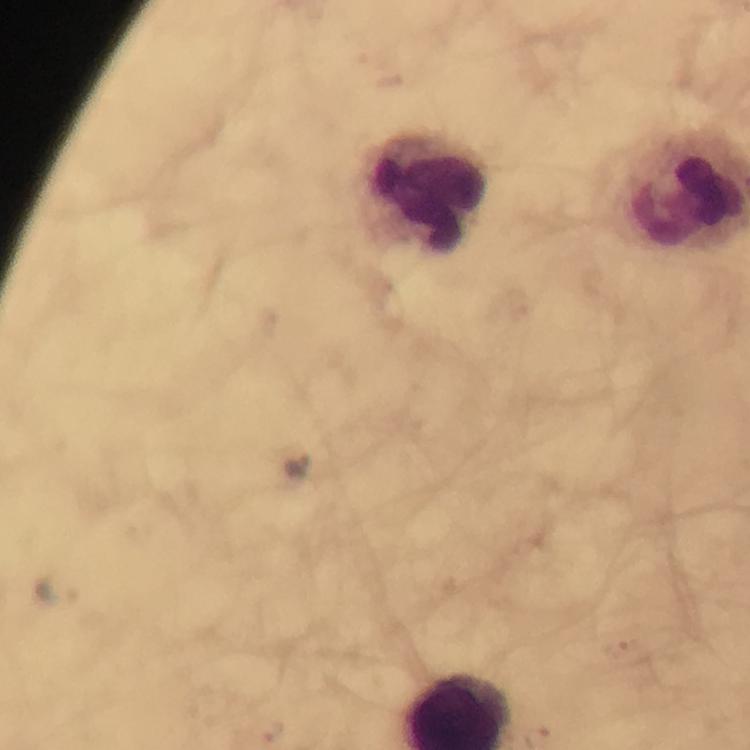
image size = 750×750 pixels
capture = smartphone camera through the microscope
preparation = thick blood smear
immersion oil = used
cropped from = one field of view
leukocyte locations = approximate object centers, in pixels from the top-left corner: (x=425, y=191)
context = from a diagnostic examination for malaria
stain = Giemsa
magnification = 100x
malaria parasite locations = approximate object centers, in pixels from the top-left corner: (x=298, y=464), (x=58, y=590), (x=619, y=645), (x=271, y=731)